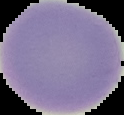
Summary:
  - Image type: segmented cell region on a black background
  - Image size: 124×115 pixels
  - Malaria status: uninfected
  - Preparation: thin blood smear